Assess this cell for malaria.
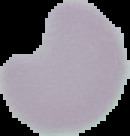
It is uninfected.

Cell region segmented out of the field of view; the surrounding area is masked to black. From a thin blood film. Image is 130×136 pixels.